Identify the blood parasite species.
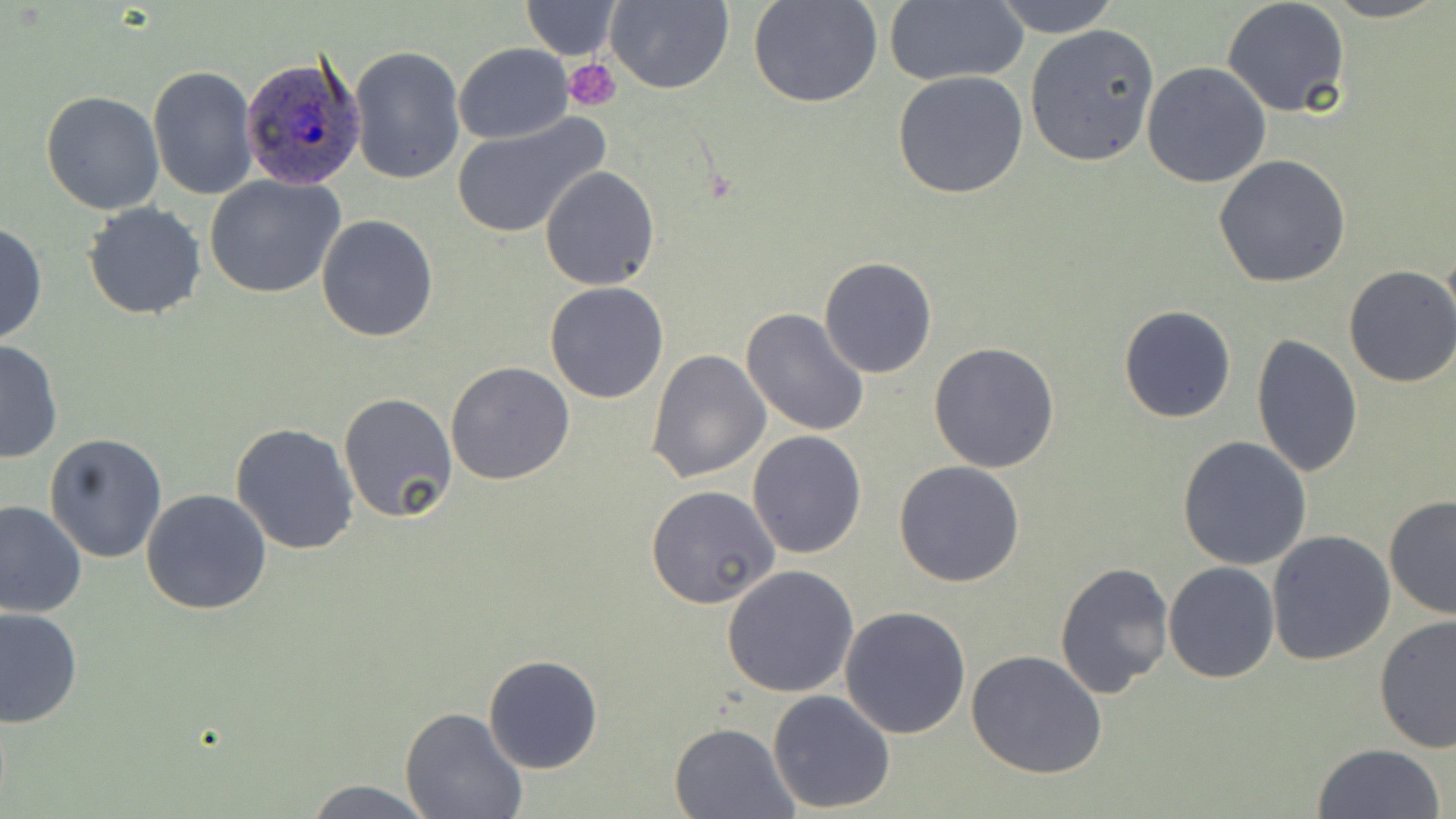

Plasmodium ovale.

field of view = single
preparation = thin blood smear
Plasmodium ovale-infected red blood cell locations = approximate bounding boxes as [x1, y1, x2, y2] in pixels: [239, 53, 365, 188]
uninfected red blood cell locations = approximate bounding boxes as [x1, y1, x2, y2] in pixels: [606, 0, 732, 93], [883, 0, 1030, 87], [991, 0, 1119, 38], [1319, 0, 1447, 22], [519, 1, 621, 59], [750, 1, 881, 108], [1221, 1, 1351, 118], [1024, 23, 1159, 168], [453, 42, 573, 145], [350, 45, 465, 183], [1141, 61, 1272, 188], [148, 66, 258, 200], [892, 71, 1029, 198], [41, 90, 164, 213], [450, 114, 610, 238], [1213, 154, 1352, 289], [540, 165, 658, 290], [203, 174, 346, 299], [81, 201, 206, 320], [316, 214, 439, 341], [0, 222, 46, 348], [819, 256, 939, 379], [1342, 265, 1456, 388], [545, 282, 669, 404], [1119, 306, 1236, 423], [740, 307, 872, 437], [1250, 334, 1363, 476], [0, 337, 62, 464], [929, 341, 1061, 472], [646, 348, 771, 483], [445, 361, 575, 485], [337, 391, 457, 523], [231, 422, 360, 555], [43, 431, 168, 562], [747, 431, 867, 559], [1177, 437, 1312, 574], [894, 461, 1025, 587], [647, 486, 781, 609], [141, 488, 272, 614], [1383, 494, 1456, 620], [0, 501, 87, 620], [1266, 529, 1397, 666], [1054, 561, 1174, 697], [1163, 561, 1281, 683], [720, 566, 860, 698], [839, 605, 971, 740], [0, 607, 82, 729], [1374, 615, 1456, 756], [967, 649, 1107, 779], [481, 654, 602, 774], [768, 690, 896, 811], [400, 708, 528, 819], [670, 720, 799, 818], [1310, 743, 1446, 819], [301, 778, 442, 817]
image size = 1456×819 pixels
platelet locations = approximate bounding boxes as [x1, y1, x2, y2] in pixels: [564, 60, 621, 111]
magnification = 1000x
stain = May-Grünwald-Giemsa
modality = light microscopy